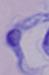
magnification = 1000x
modality = photomicrograph
identification = trypanosome